Locate every blood parasite and identify its species.
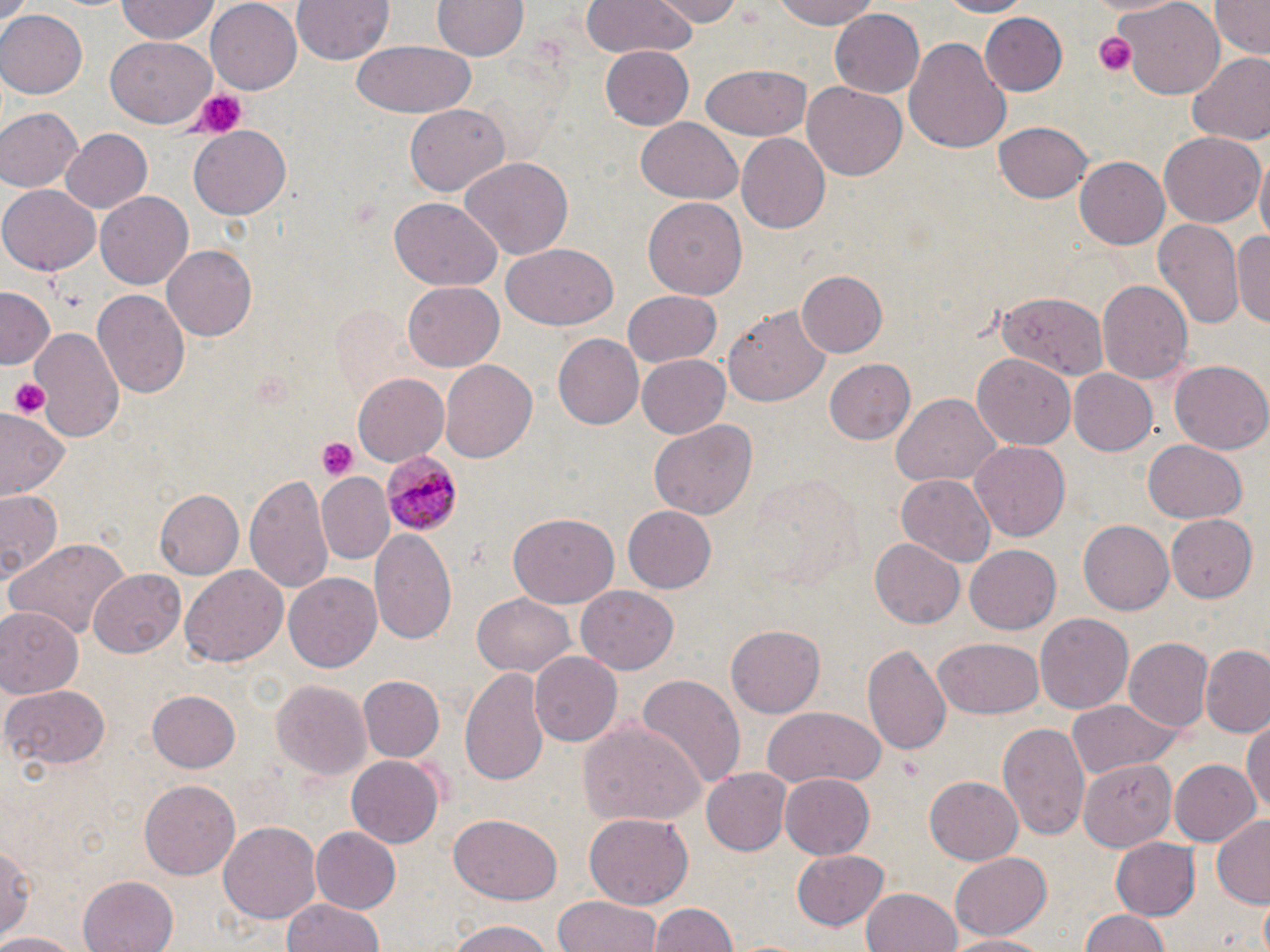

Approximate bounding boxes as (x1,y1)-(x2,y2) corner pairs in pixels.
Plasmodium malariae-infected red blood cells: (378,453)-(463,535).
No Plasmodium falciparum, Plasmodium ovale, Plasmodium vivax, Babesia divergens, or Trypanosoma brucei observed.

Summary:
  - Platelet locations: (1094,30)-(1137,76), (188,88)-(249,140), (8,377)-(51,418), (316,438)-(357,480)
  - Uninfected red blood cell locations: (289,0)-(395,65), (581,0)-(697,57), (656,0)-(742,25), (771,0)-(882,30), (929,0)-(1032,17), (1086,0)-(1184,18), (1210,0)-(1268,57), (115,1)-(222,44), (206,1)-(303,92), (433,1)-(525,61), (1117,1)-(1227,97), (831,8)-(925,98), (0,10)-(85,100), (982,13)-(1066,94), (903,36)-(1011,155), (106,37)-(218,128), (353,40)-(477,118), (600,44)-(695,129), (1186,50)-(1270,146), (701,65)-(811,140), (802,80)-(907,181), (405,103)-(509,197), (0,107)-(82,194), (635,118)-(743,204), (993,122)-(1093,204), (191,128)-(290,216), (59,130)-(152,213), (1159,130)-(1265,227), (737,134)-(830,235), (457,155)-(571,258), (1074,157)-(1168,250), (1254,157)-(1269,249), (0,184)-(100,274), (96,191)-(194,289), (642,198)-(749,301), (389,199)-(503,290), (1152,218)-(1244,334), (1234,223)-(1270,333), (163,244)-(259,341), (501,244)-(619,330), (797,271)-(888,358), (1097,279)-(1192,386), (402,283)-(503,371), (0,288)-(53,371), (92,289)-(189,399), (622,291)-(722,368), (995,291)-(1110,380), (726,305)-(832,406), (32,327)-(122,443), (550,330)-(644,428), (972,352)-(1074,448), (636,355)-(730,437), (823,357)-(916,446), (439,359)-(536,465), (1170,361)-(1270,455), (1067,368)-(1159,456), (353,372)-(449,467), (891,393)-(1000,488), (2,411)-(69,500), (649,420)-(757,519), (1144,439)-(1247,522), (970,440)-(1071,541), (318,473)-(390,560), (245,474)-(331,592), (898,474)-(997,567), (0,488)-(65,581), (152,489)-(243,579), (622,504)-(717,594), (1166,514)-(1258,602), (508,515)-(618,607), (1079,520)-(1175,614), (371,527)-(457,642), (6,537)-(130,637), (869,538)-(965,628), (967,547)-(1061,633), (180,566)-(286,668), (88,570)-(184,658), (284,571)-(382,671), (574,586)-(676,674), (473,593)-(577,677), (0,605)-(81,695), (1035,613)-(1133,715), (727,626)-(824,716), (932,636)-(1044,719), (1121,638)-(1212,732), (864,644)-(950,758), (1201,648)-(1270,738), (530,651)-(621,746), (459,666)-(550,790), (639,674)-(748,786), (358,676)-(445,763), (270,678)-(372,779), (3,683)-(112,769), (149,690)-(241,772), (1068,701)-(1183,778), (760,707)-(887,790), (1245,718)-(1270,821), (580,719)-(706,830), (999,722)-(1088,840), (345,754)-(444,847), (1078,758)-(1180,877), (1168,758)-(1260,848), (702,769)-(792,853), (779,770)-(875,859), (925,776)-(1023,863), (139,778)-(242,879), (584,810)-(695,909), (450,813)-(563,904), (1212,814)-(1270,907), (220,822)-(320,921), (309,826)-(402,915), (2,836)-(36,942), (1111,838)-(1201,917), (790,849)-(890,932), (950,852)-(1054,940), (77,874)-(178,952), (861,886)-(962,952), (553,896)-(664,952), (281,898)-(384,952), (1255,898)-(1270,952), (648,901)-(736,952), (1080,909)-(1170,952), (445,920)-(554,952), (0,931)-(85,952), (951,931)-(1049,952)
  - Slide-level diagnosis: Plasmodium malariae
  - Modality: light microscopy
  - Image size: 1270×952 pixels
  - Stain: May-Grünwald-Giemsa
  - Magnification: 1000x
  - Preparation: thin blood film
  - Field of view: single